Report the malaria status of this cell.
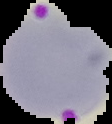
It is parasitized.

Summary:
  - Image size: 112×124 pixels
  - Preparation: thin blood smear
  - Image type: cell region segmented out of the field of view; surrounding area masked to black